Outline each blood parasite and name the species.
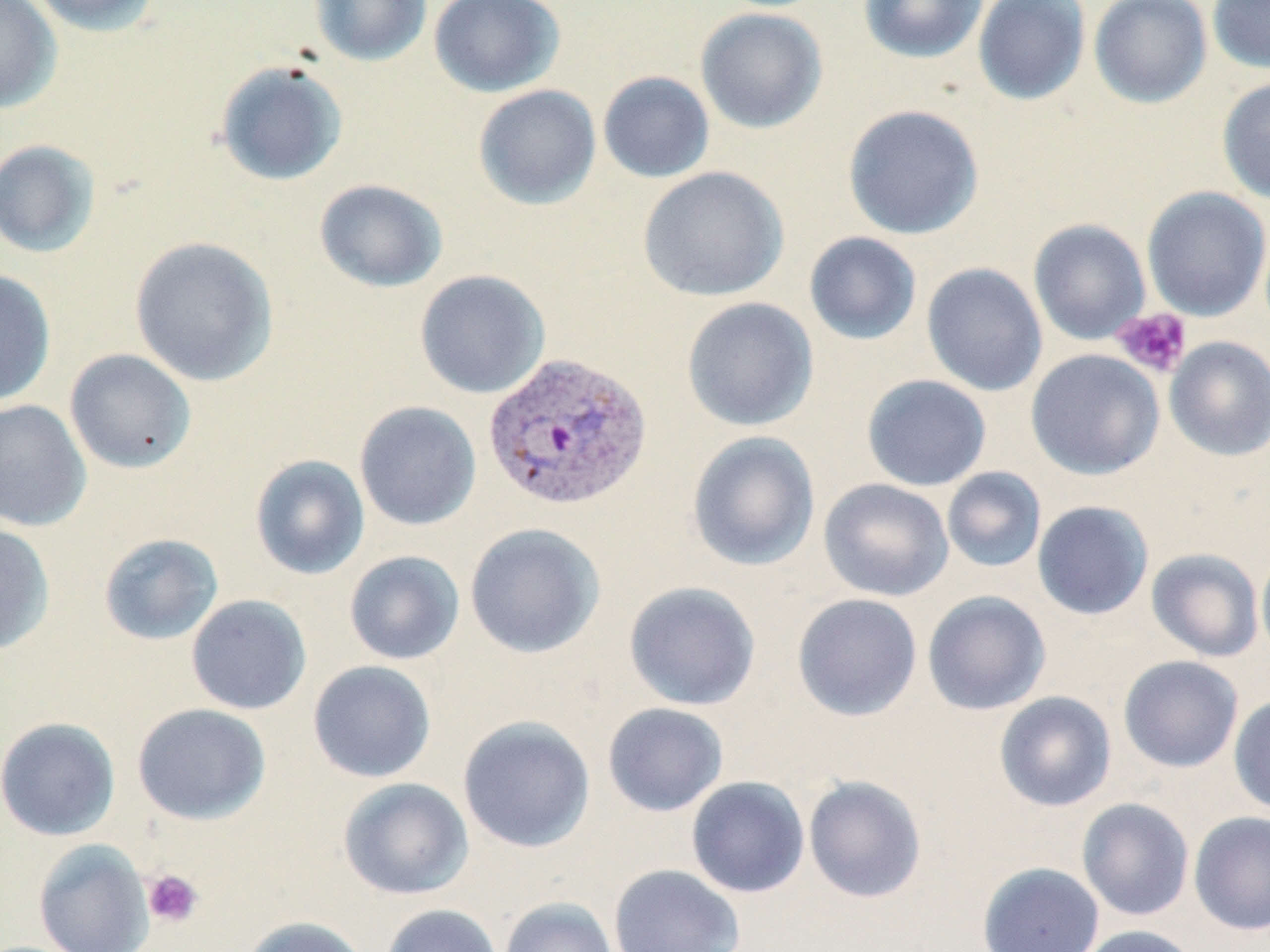
Approximate bounding boxes as [x1, y1, x2, y2] in pixels.
Plasmodium vivax-infected red blood cells: [482, 350, 653, 512].
No Plasmodium falciparum, Plasmodium ovale, Plasmodium malariae, Babesia divergens, or Trypanosoma brucei observed.

Summary:
  - Platelet locations: [1111, 308, 1192, 378], [142, 869, 204, 928]
  - Uninfected red blood cell locations: [0, 0, 62, 114], [26, 0, 162, 36], [309, 0, 433, 67], [428, 0, 565, 98], [858, 0, 988, 63], [972, 0, 1091, 105], [1088, 0, 1212, 108], [1207, 0, 1270, 75], [695, 8, 828, 134], [214, 61, 348, 186], [598, 71, 715, 183], [1216, 75, 1270, 205], [473, 84, 602, 210], [842, 104, 984, 240], [0, 139, 100, 258], [637, 166, 789, 302], [314, 179, 448, 292], [1141, 186, 1270, 321], [1028, 219, 1151, 345], [803, 231, 922, 345], [128, 236, 279, 387], [921, 262, 1048, 396], [0, 268, 57, 408], [414, 269, 550, 399], [681, 297, 818, 432], [1164, 336, 1270, 461], [64, 348, 197, 474], [1026, 349, 1165, 480], [861, 374, 992, 491], [0, 399, 91, 532], [354, 400, 481, 531], [686, 431, 820, 572], [249, 454, 370, 580], [941, 467, 1047, 573], [818, 478, 954, 602], [1032, 500, 1154, 620], [0, 522, 55, 655], [464, 522, 605, 659], [98, 532, 224, 646], [1256, 547, 1270, 663], [1146, 548, 1264, 662], [344, 550, 465, 665], [623, 581, 761, 710], [922, 590, 1051, 715], [792, 593, 922, 722], [185, 594, 312, 715], [1118, 655, 1244, 773], [307, 660, 436, 783], [994, 691, 1117, 812], [1228, 694, 1270, 817], [602, 702, 729, 817], [132, 703, 271, 825], [458, 716, 596, 853], [0, 717, 121, 841], [803, 775, 927, 904], [686, 776, 810, 898], [337, 777, 474, 900], [1076, 798, 1195, 921], [1189, 811, 1270, 936], [33, 839, 154, 952], [977, 862, 1105, 952], [608, 863, 746, 952], [499, 896, 620, 952], [380, 903, 503, 952], [241, 915, 370, 952], [1073, 924, 1203, 952]
  - Slide-level diagnosis: Plasmodium vivax
  - Preparation: thin blood film
  - Magnification: 1000x
  - Field of view: single
  - Stain: May-Grünwald-Giemsa
  - Modality: light microscopy
  - Image size: 1270×952 pixels